Report the malaria status of this cell.
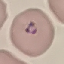

It is parasitized.

Thin blood smear. Cell patch, automatically extracted from a larger field of view and resized to 64 × 64 pixels. Photographed with a smartphone camera at the microscope eyepiece. Giemsa stain.